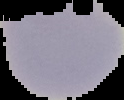
Summary:
  - Image type: cell region segmented out of the field of view; surrounding area masked to black
  - Image size: 124×100 pixels
  - Malaria status: parasitized
  - Preparation: thin blood film